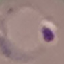

result = malaria parasites detected
preparation = thin smear
image type = automatically extracted cell patch, resized to 64 × 64 pixels
stain = Giemsa
capture = smartphone through the microscope eyepiece